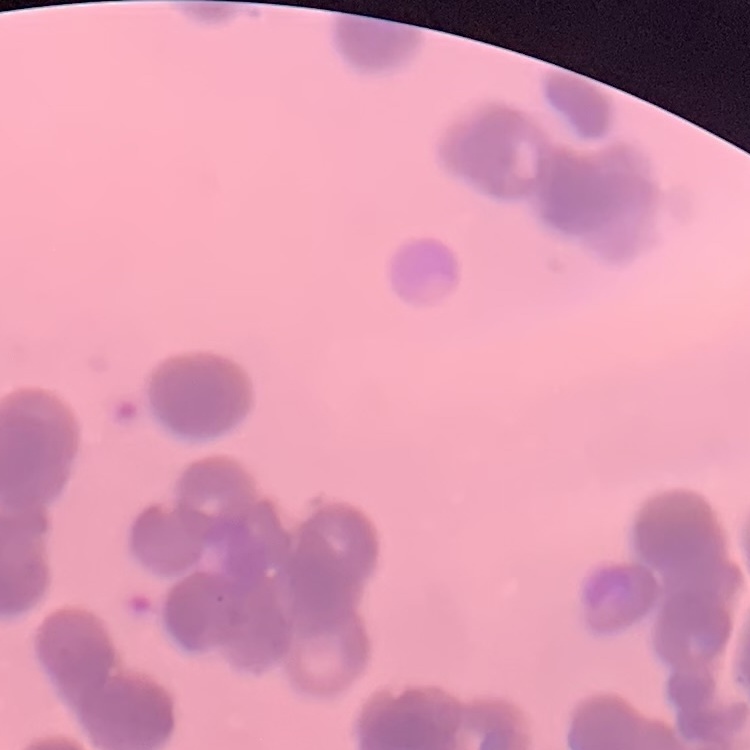

The erythrocytes exhibit rouleaux formation. Stained with either Field's or Giemsa. One tile cut from a larger photomicrograph. Thin blood film.